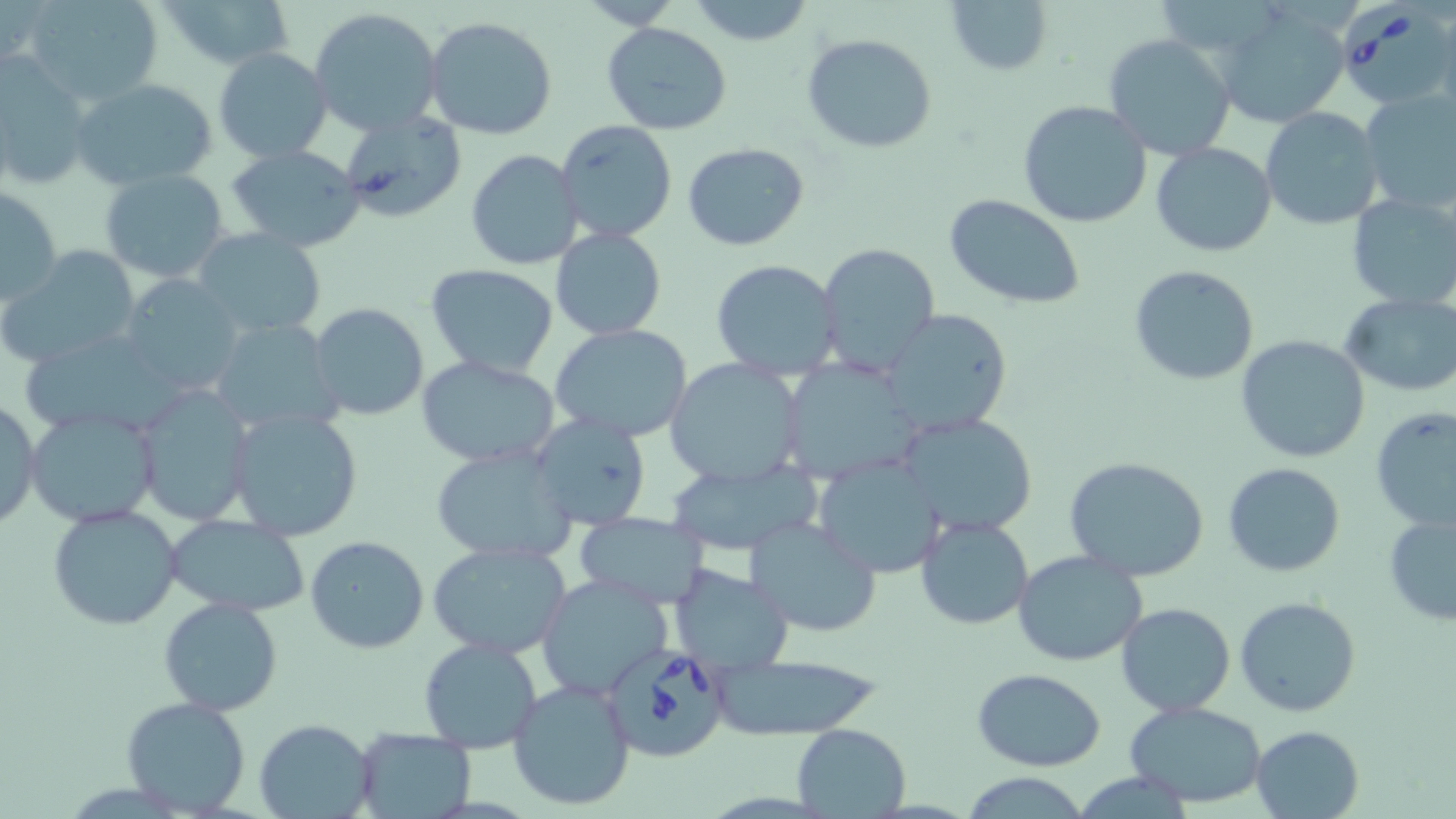

Summary:
  - Coordinate format: approximate bounding boxes as (x1, y1, x2, y2) in pixels
  - Babesia divergens-infected red blood cell locations: (1337, 2, 1456, 111), (602, 642, 732, 762)
  - Uninfected red blood cell locations: (24, 0, 165, 107), (154, 0, 297, 69), (942, 0, 1053, 76), (570, 1, 683, 30), (685, 1, 818, 48), (1216, 5, 1354, 128), (309, 7, 443, 135), (425, 15, 560, 141), (602, 21, 733, 134), (216, 29, 433, 148), (802, 31, 938, 154), (1103, 34, 1237, 160), (213, 48, 334, 163), (0, 54, 93, 192), (69, 77, 218, 193), (1356, 89, 1456, 216), (1017, 100, 1152, 229), (1260, 107, 1384, 229), (339, 108, 467, 223), (554, 120, 677, 244), (1151, 141, 1276, 257), (683, 142, 811, 252), (225, 143, 369, 252), (466, 148, 584, 270), (100, 167, 231, 284), (2, 185, 65, 308), (1345, 193, 1456, 310), (943, 195, 1087, 309), (194, 227, 325, 337), (550, 228, 668, 342), (815, 242, 942, 374), (1, 247, 142, 369), (710, 258, 844, 380), (425, 263, 559, 380), (1128, 264, 1261, 386), (121, 275, 247, 397), (1340, 294, 1456, 397), (309, 302, 430, 422), (882, 308, 1016, 437), (210, 318, 341, 440), (549, 324, 697, 443), (1235, 334, 1372, 463), (415, 354, 561, 468), (781, 357, 926, 486), (664, 358, 808, 487), (132, 386, 255, 527), (0, 396, 42, 532), (24, 405, 161, 528), (1371, 406, 1456, 531), (224, 407, 367, 541), (529, 411, 652, 532), (898, 411, 1041, 537), (429, 444, 580, 567), (813, 453, 946, 579), (667, 455, 818, 557), (1063, 455, 1210, 582), (1223, 463, 1347, 578), (48, 504, 184, 631), (1383, 509, 1456, 628), (574, 510, 710, 606), (165, 514, 310, 617), (915, 515, 1036, 630), (745, 517, 883, 637), (305, 535, 430, 653), (428, 540, 571, 659), (1012, 550, 1148, 668), (669, 564, 795, 671), (537, 573, 674, 702), (1234, 595, 1362, 717), (158, 597, 284, 717), (1116, 602, 1236, 716), (419, 637, 544, 754), (698, 655, 889, 740), (973, 668, 1106, 772), (507, 679, 636, 810), (120, 695, 252, 817), (1122, 700, 1270, 805), (255, 718, 374, 819), (791, 723, 910, 817), (1250, 724, 1364, 818), (354, 725, 478, 817)
  - Slide-level diagnosis: Babesia divergens
  - Preparation: thin blood smear
  - Stain: May-Grünwald-Giemsa
  - Magnification: 1000x
  - Field of view: single
  - Image size: 1456×819 pixels
  - Modality: optical microscopy